Report the malaria status of this cell.
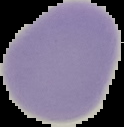
It is uninfected.

{
  "image_type": "segmented cell region with the area outside set to black",
  "preparation": "thin blood smear",
  "image_size": "124×127 pixels"
}